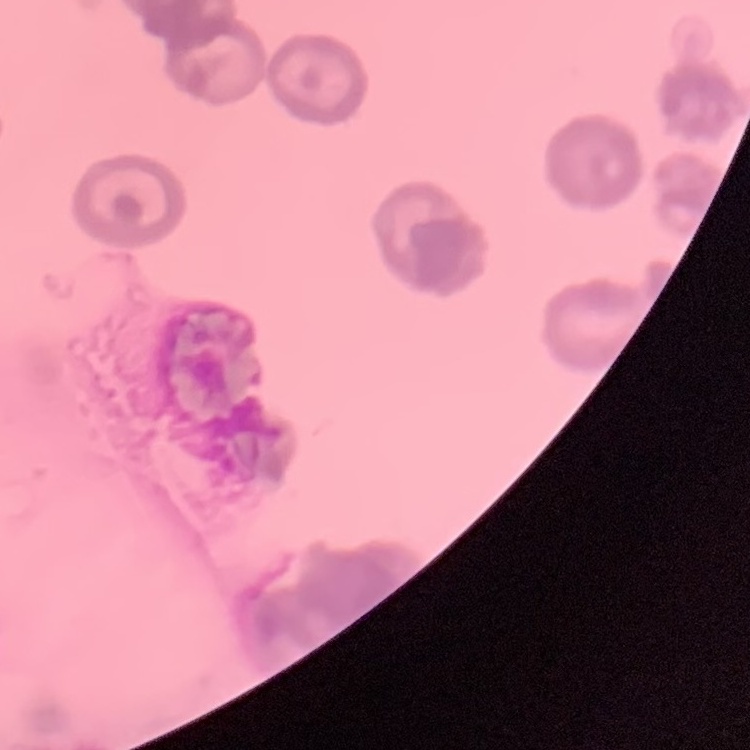
erythrocyte morphology = rouleaux formation
image type = square crop of a larger photomicrograph
preparation = thin blood film
stain = Field's or Giemsa